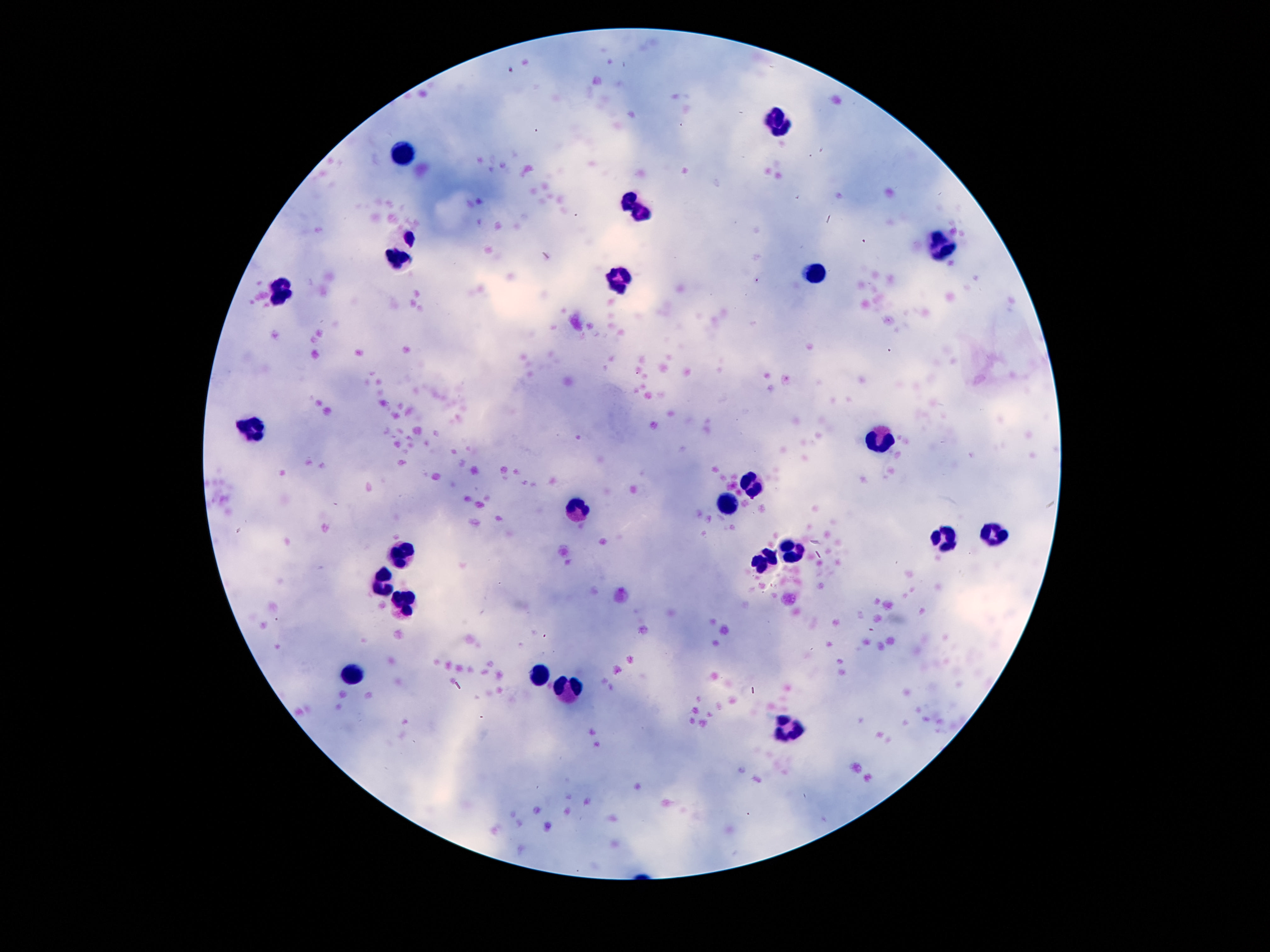
Approximate centers as [x, y] in pixels. Leukocyte locations: [777, 124], [404, 156], [638, 209], [939, 245], [399, 251], [814, 273], [620, 283], [281, 291], [257, 427], [880, 439], [751, 483], [727, 504], [573, 511], [994, 533], [942, 539], [792, 549], [401, 554], [763, 561], [381, 588], [401, 607], [538, 675], [352, 678], [569, 687], [787, 729]. Patient malaria status: uninfected. 100x magnification. Image is 1270×952 pixels. Smartphone photograph taken through the microscope eyepiece. Giemsa stain. Single field of view. Thick blood film.